Locate every blood parasite and identify its species.
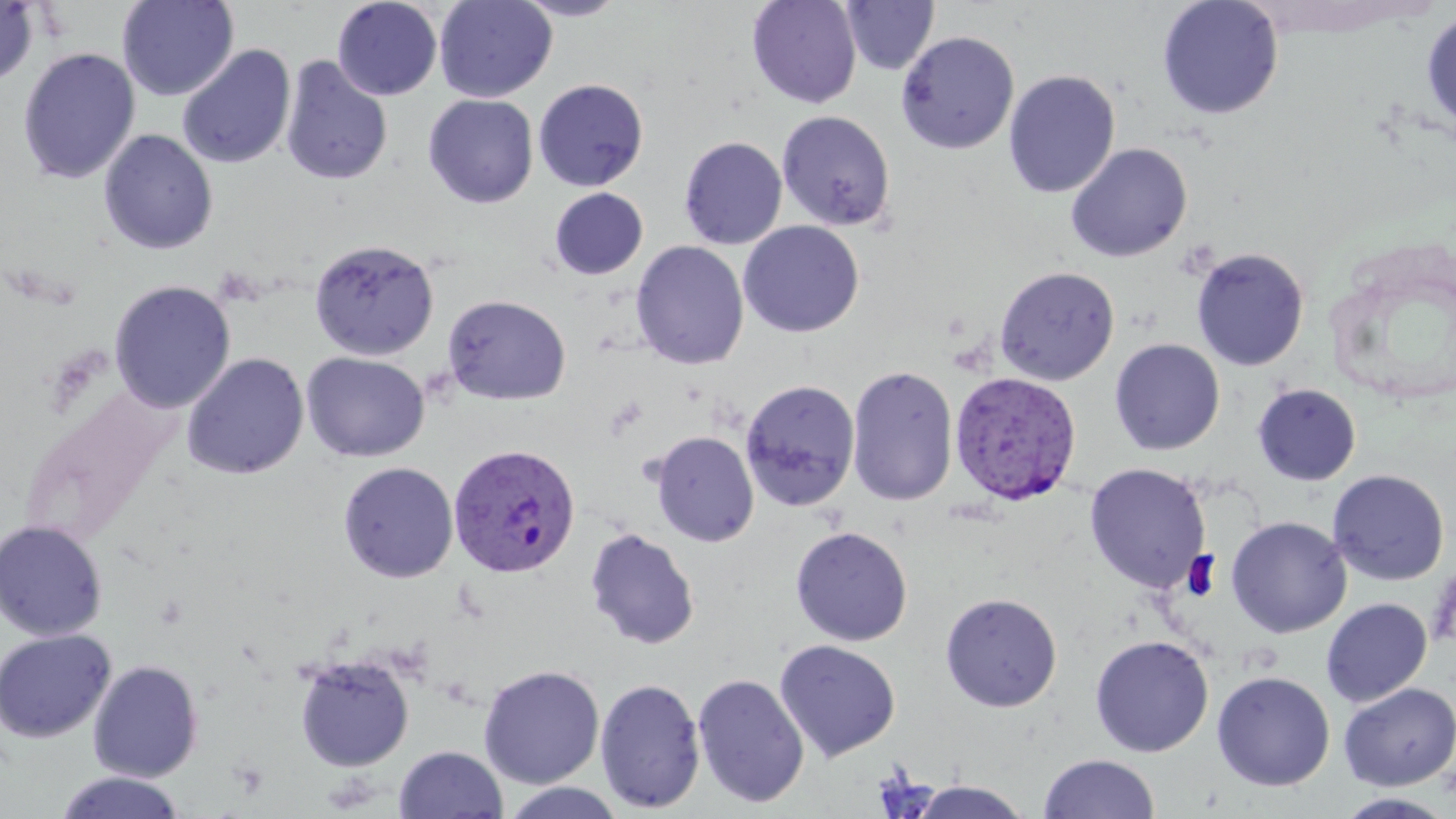
Approximate bounding boxes as named x1/y1/x2/y2 corners in pixels.
Plasmodium vivax-infected red blood cells: (x1=948, y1=370, x2=1084, y2=507), (x1=447, y1=442, x2=582, y2=579).
No Plasmodium falciparum, Plasmodium ovale, Plasmodium malariae, Babesia divergens, or Trypanosoma brucei observed.

Summary:
  - Uninfected red blood cell locations: (x1=117, y1=0, x2=239, y2=101), (x1=332, y1=0, x2=443, y2=101), (x1=434, y1=0, x2=558, y2=103), (x1=511, y1=0, x2=630, y2=22), (x1=746, y1=0, x2=862, y2=109), (x1=1157, y1=0, x2=1284, y2=120), (x1=840, y1=1, x2=940, y2=76), (x1=0, y1=2, x2=38, y2=88), (x1=1421, y1=8, x2=1456, y2=135), (x1=896, y1=30, x2=1019, y2=154), (x1=176, y1=44, x2=296, y2=170), (x1=17, y1=47, x2=141, y2=184), (x1=279, y1=56, x2=393, y2=186), (x1=1003, y1=70, x2=1120, y2=198), (x1=533, y1=78, x2=649, y2=192), (x1=423, y1=94, x2=539, y2=209), (x1=776, y1=110, x2=896, y2=231), (x1=99, y1=129, x2=218, y2=255), (x1=678, y1=136, x2=787, y2=250), (x1=1065, y1=143, x2=1192, y2=263), (x1=549, y1=187, x2=648, y2=280), (x1=738, y1=220, x2=864, y2=338), (x1=309, y1=238, x2=439, y2=361), (x1=630, y1=241, x2=749, y2=370), (x1=1190, y1=247, x2=1310, y2=371), (x1=994, y1=265, x2=1120, y2=386), (x1=109, y1=280, x2=235, y2=413), (x1=442, y1=294, x2=572, y2=406), (x1=1109, y1=338, x2=1226, y2=455), (x1=301, y1=352, x2=430, y2=462), (x1=181, y1=353, x2=309, y2=481), (x1=846, y1=365, x2=958, y2=506), (x1=740, y1=379, x2=861, y2=511), (x1=1252, y1=383, x2=1362, y2=486), (x1=650, y1=430, x2=759, y2=547), (x1=338, y1=462, x2=459, y2=583), (x1=1084, y1=463, x2=1211, y2=593), (x1=1327, y1=469, x2=1450, y2=586), (x1=1226, y1=515, x2=1351, y2=638), (x1=0, y1=519, x2=108, y2=641), (x1=790, y1=526, x2=913, y2=646), (x1=585, y1=527, x2=700, y2=650), (x1=940, y1=592, x2=1062, y2=712), (x1=1321, y1=598, x2=1432, y2=706), (x1=0, y1=628, x2=116, y2=743), (x1=1090, y1=634, x2=1214, y2=757), (x1=773, y1=639, x2=900, y2=762), (x1=294, y1=653, x2=415, y2=771), (x1=88, y1=660, x2=203, y2=782), (x1=478, y1=664, x2=605, y2=789), (x1=1212, y1=670, x2=1335, y2=791), (x1=692, y1=673, x2=810, y2=809), (x1=594, y1=678, x2=706, y2=813), (x1=1338, y1=682, x2=1456, y2=790), (x1=395, y1=745, x2=508, y2=818), (x1=1037, y1=753, x2=1159, y2=819), (x1=55, y1=771, x2=187, y2=819), (x1=908, y1=780, x2=1035, y2=817), (x1=499, y1=782, x2=629, y2=819), (x1=1333, y1=792, x2=1456, y2=818)
  - Slide-level diagnosis: Plasmodium vivax
  - Modality: optical microscopy
  - Stain: May-Grünwald-Giemsa
  - Preparation: thin blood film
  - Field of view: one of a larger specimen
  - Magnification: 1000x
  - Image size: 1456×819 pixels